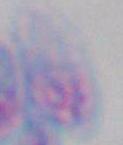
modality = micrograph
magnification = 1000x
identification = Toxoplasma gondii